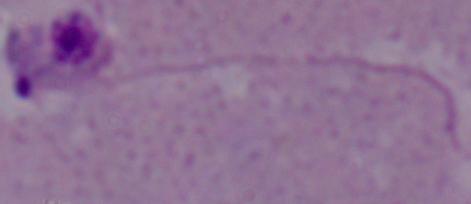
Summary:
  - Modality: micrograph
  - Magnification: 1000x
  - Identification: Leishmania